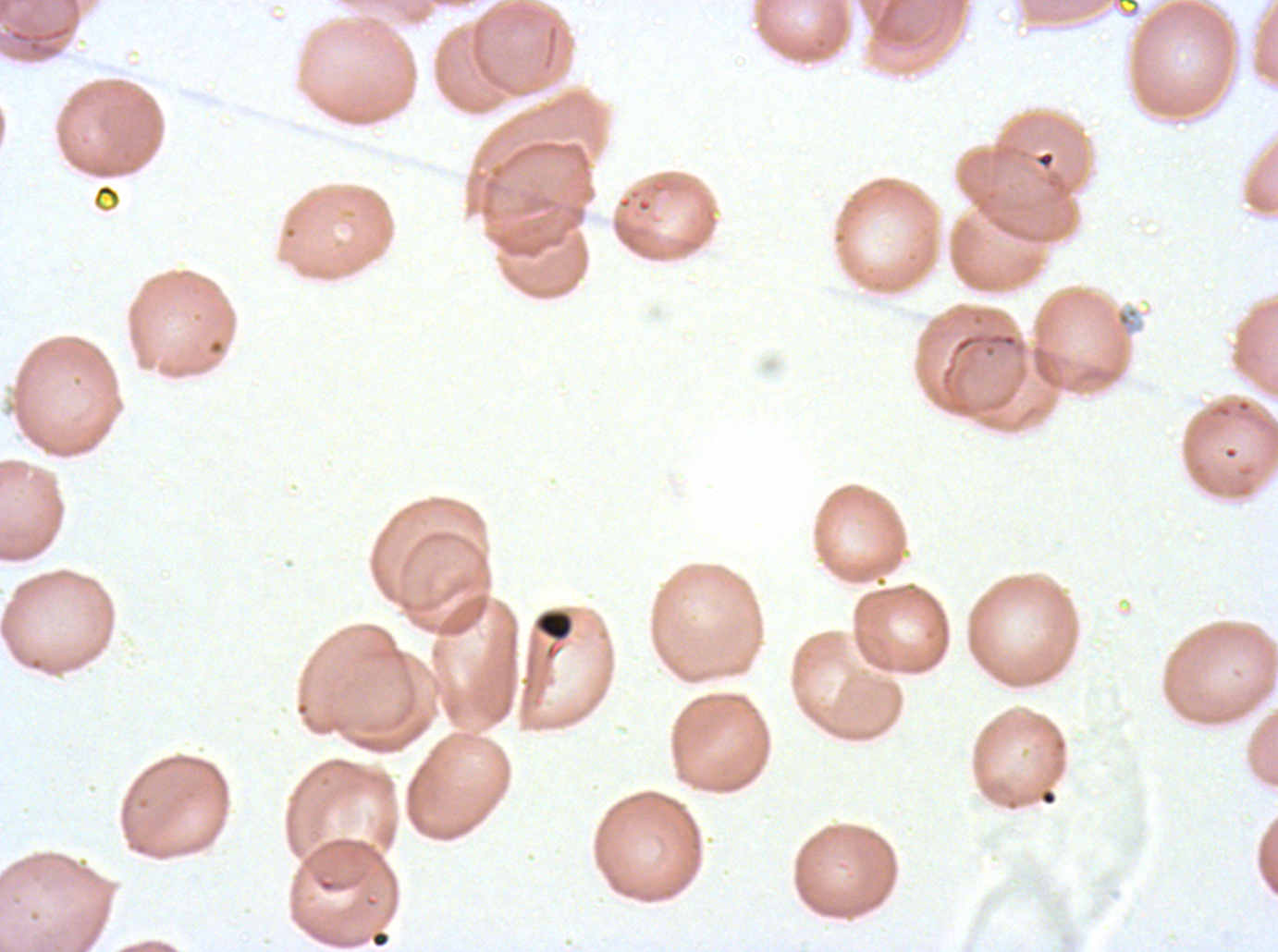

Approximate bounding rectangles given as corner coordinates in pixels from the top-left.
Summary:
  - Debris locations: (x1=535, y1=609, x2=573, y2=641)
  - Stain: Giemsa
  - Specimen: Plasmodium falciparum cultured ex vivo for 24 to 48 hours, from a patient in The Gambia
  - Field of view: one sub-image of a larger composite
  - Image size: 1278×952 pixels
  - Preparation: thin blood smear